Report the malaria status of this cell.
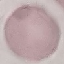

It is uninfected.

Acquired by smartphone through the microscope eyepiece. Thin blood smear. Giemsa stain. Cell patch, automatically extracted from a larger field of view and resized to 64 × 64 pixels.